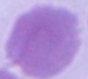

modality: photomicrograph
identification: erythrocyte
magnification: 1000x